Report the malaria status of this cell.
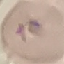
It is uninfected.

Summary:
  - Capture: smartphone camera at the microscope eyepiece
  - Preparation: thin blood film
  - Stain: Giemsa
  - Image type: cell patch, automatically extracted from a larger field of view and resized to 64 × 64 pixels